Report the malaria status of this cell.
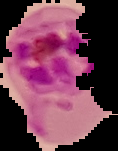

Parasitized.

From a thin blood smear. Image is 118×151 pixels. Segmented cell region on a black background.